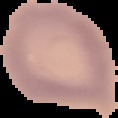 Cell region segmented out of the field of view; the surrounding area is masked to black. From a thin blood film. Image is 118×118 pixels. Malaria status: uninfected.